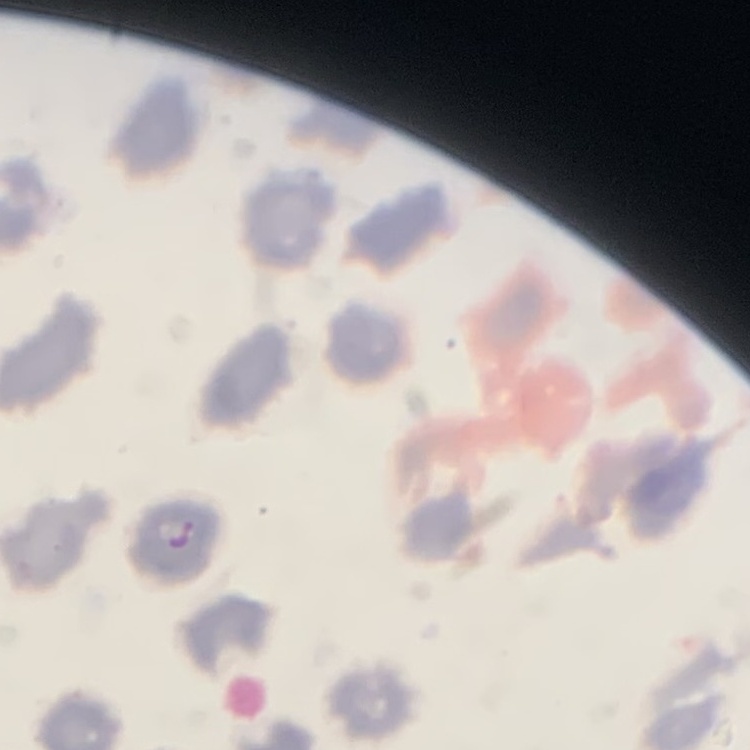

{
  "erythrocyte_morphology": "no rouleaux formation",
  "image_type": "square crop of a larger photomicrograph",
  "preparation": "thin peripheral smear",
  "stain": "Field's or Giemsa"
}